Give the extent of all Plasmodium falciparum-infected red blood cells.
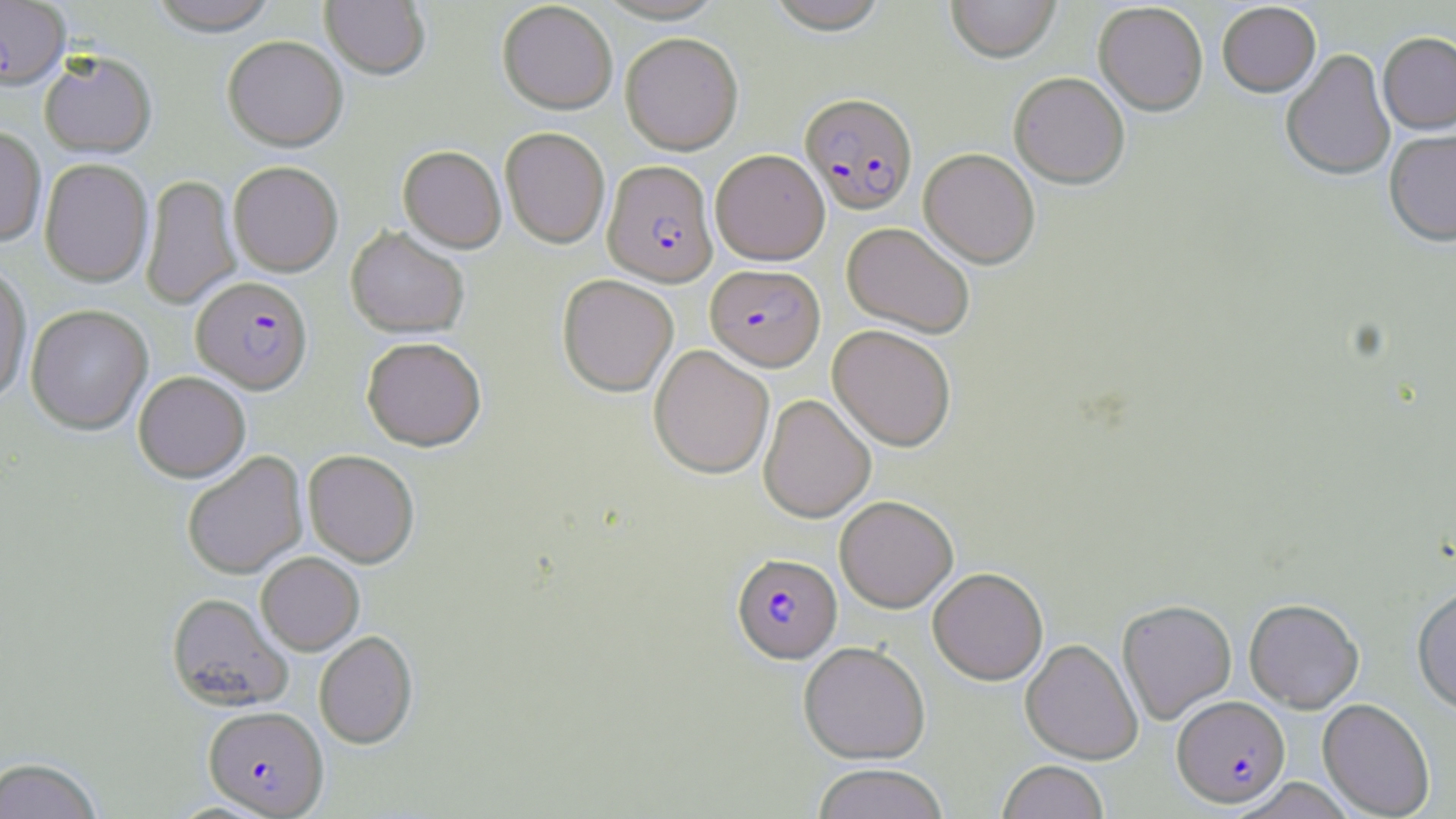
Approximate bounding boxes as (x1, y1, x2, y2) in pixels.
Plasmodium falciparum-infected red blood cells: (0, 1, 69, 91), (801, 92, 918, 214), (603, 160, 718, 286), (706, 264, 826, 371), (191, 276, 313, 395), (732, 552, 841, 663), (1172, 695, 1290, 806), (203, 706, 329, 817).

{
  "slide_level_diagnosis": "Plasmodium falciparum",
  "image_size": "1456×819 pixels",
  "preparation": "thin blood film",
  "stain": "May-Grünwald-Giemsa",
  "uninfected_red_blood_cell_locations": "approximate bounding boxes as (x1, y1, x2, y2) in pixels: (148, 0, 279, 37), (320, 0, 430, 80), (593, 0, 729, 24), (765, 0, 891, 35), (945, 0, 1061, 63), (497, 2, 617, 114), (1094, 3, 1208, 116), (1217, 3, 1321, 98), (620, 32, 744, 154), (1378, 33, 1456, 136), (223, 37, 348, 151), (1281, 49, 1395, 182), (39, 52, 157, 159), (1009, 72, 1130, 188), (0, 127, 46, 246), (500, 127, 610, 248), (1384, 132, 1456, 248), (398, 146, 506, 253), (919, 148, 1040, 268), (710, 149, 830, 265), (39, 158, 153, 287), (229, 161, 342, 276), (141, 175, 240, 309), (842, 222, 975, 338), (346, 226, 470, 338), (0, 265, 32, 404), (557, 275, 678, 396), (25, 304, 153, 435), (828, 324, 956, 451), (362, 337, 487, 451), (649, 345, 774, 479), (133, 372, 251, 482), (758, 394, 876, 523), (303, 450, 420, 568), (182, 451, 308, 579), (834, 495, 958, 612), (256, 552, 364, 655), (928, 567, 1048, 685), (1412, 585, 1456, 716), (166, 592, 294, 712), (1117, 599, 1236, 724), (1244, 599, 1364, 712), (314, 631, 417, 749), (1020, 639, 1142, 764), (798, 641, 930, 764), (1317, 698, 1435, 818), (0, 757, 102, 818), (997, 760, 1109, 819), (811, 763, 950, 819)",
  "modality": "optical microscopy",
  "magnification": "1000x",
  "field_of_view": "single"
}